Classify this cell by malaria status.
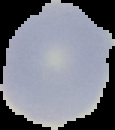

It is uninfected.

Summary:
  - Image size: 115×130 pixels
  - Image type: cell region segmented out of the field of view; surrounding area masked to black
  - Preparation: thin blood film